Give the position of every Plasmodium parasite.
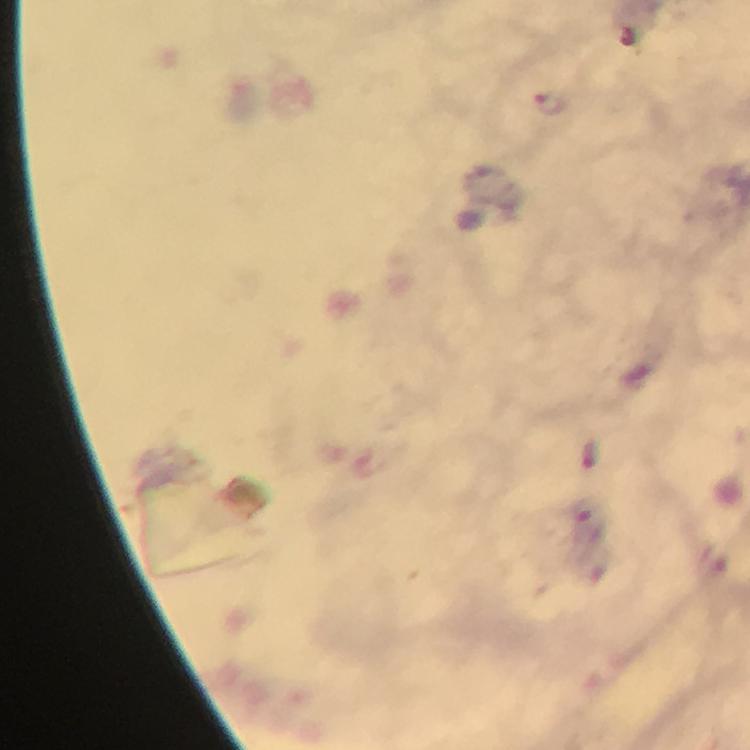

Approximate centers as [x, y] in pixels.
Plasmodium parasites: [553, 106].

Summary:
  - Magnification: 100x
  - Preparation: thick blood film
  - Cropped from: one field of view
  - Context: from a malaria diagnostic workup
  - Capture: smartphone camera through the microscope
  - Stain: Giemsa
  - Image size: 750×750 pixels
  - Immersion oil: applied